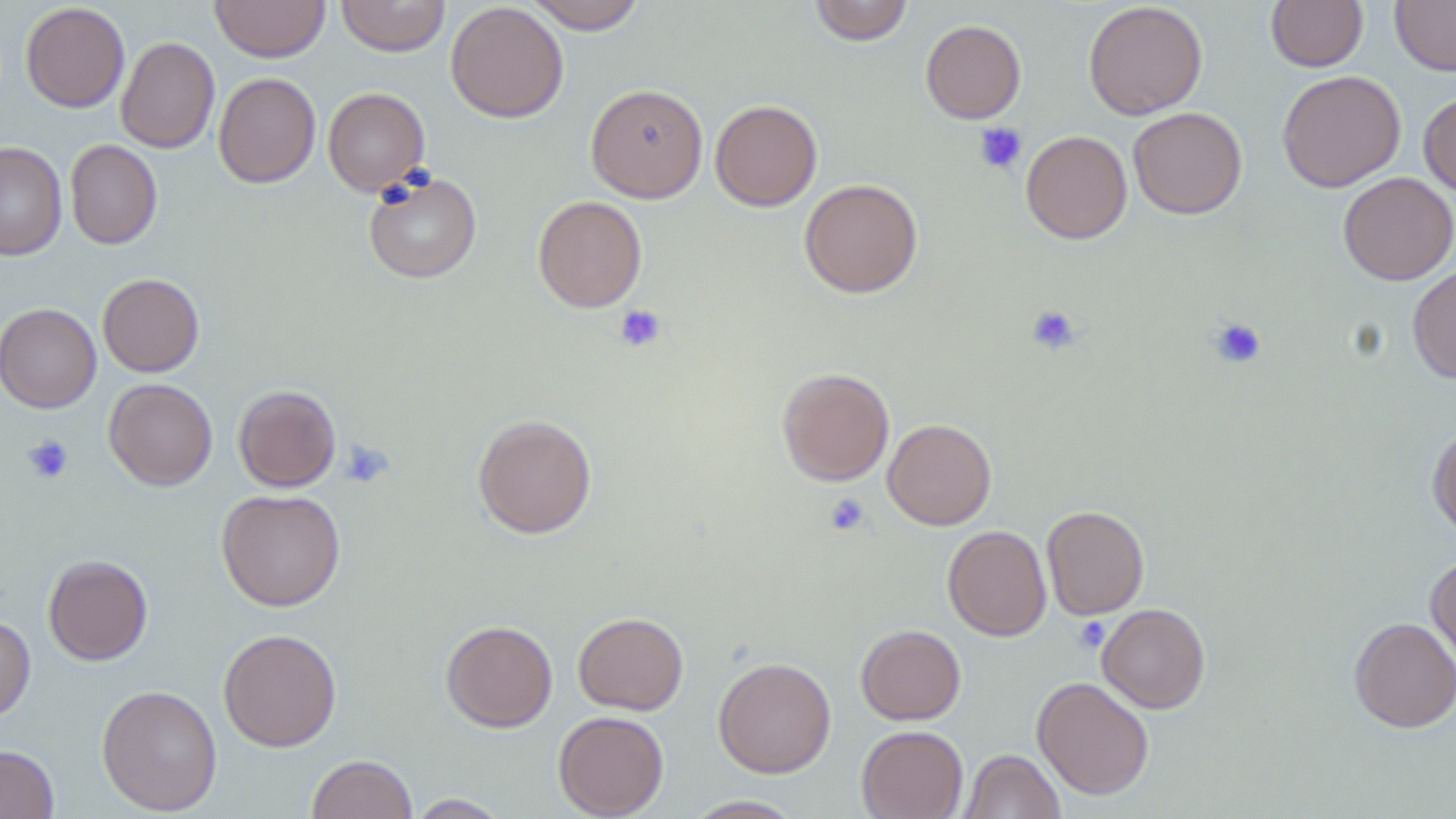
Summary:
  - Coordinate format: approximate bounding boxes as (x1,y1)-(x2,y2) corner pairs in pixels
  - Platelet locations: (974,122)-(1028,175), (614,304)-(666,352), (1027,304)-(1081,354), (1209,318)-(1266,368), (22,434)-(74,484), (339,439)-(395,488), (824,494)-(870,536), (1073,617)-(1110,652)
  - Uninfected red blood cell locations: (210,0)-(329,62), (336,0)-(451,57), (523,0)-(647,33), (809,0)-(913,45), (1266,0)-(1368,72), (1390,0)-(1456,75), (445,1)-(569,123), (1083,1)-(1208,120), (20,2)-(130,112), (921,20)-(1026,123), (116,36)-(220,154), (1277,69)-(1406,192), (213,72)-(321,188), (585,83)-(708,203), (323,87)-(430,195), (1418,90)-(1456,196), (709,99)-(823,211), (1128,106)-(1247,219), (1021,130)-(1132,243), (65,140)-(162,249), (0,141)-(67,261), (363,170)-(482,283), (1337,172)-(1456,285), (799,178)-(923,297), (533,195)-(647,313), (1407,264)-(1456,383), (97,273)-(204,377), (0,303)-(101,412), (777,367)-(894,486), (104,379)-(218,490), (233,385)-(341,492), (473,414)-(597,538), (882,418)-(996,530), (1427,424)-(1456,540), (215,488)-(346,611), (1041,505)-(1150,620), (943,525)-(1051,641), (43,554)-(153,665), (1425,554)-(1456,672), (1097,603)-(1211,713), (573,612)-(688,715), (0,615)-(36,724), (1349,616)-(1456,732), (441,620)-(558,732), (855,624)-(966,725), (218,628)-(342,751), (713,657)-(837,778), (1032,676)-(1154,799), (96,684)-(223,816), (553,710)-(669,818), (856,725)-(968,819), (0,744)-(59,819), (960,749)-(1065,819), (306,754)-(418,819), (405,794)-(510,818), (683,795)-(805,818)
  - Slide-level diagnosis: no evidence of blood parasites
  - Image size: 1456×819 pixels
  - Preparation: thin blood film
  - Stain: May-Grünwald-Giemsa
  - Modality: light microscopy
  - Field of view: single
  - Magnification: 1000x